Assess this cell for malaria.
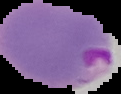

Parasitized.

Summary:
  - Image size: 121×94 pixels
  - Preparation: thin blood smear
  - Image type: cell region segmented out of the field of view; surrounding area masked to black